Assess this cell for malaria.
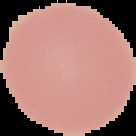

It is uninfected.

image_type: segmented cell region with the area outside set to black
preparation: thin blood film
image_size: 136×136 pixels